Describe the morphology of the erythrocytes.
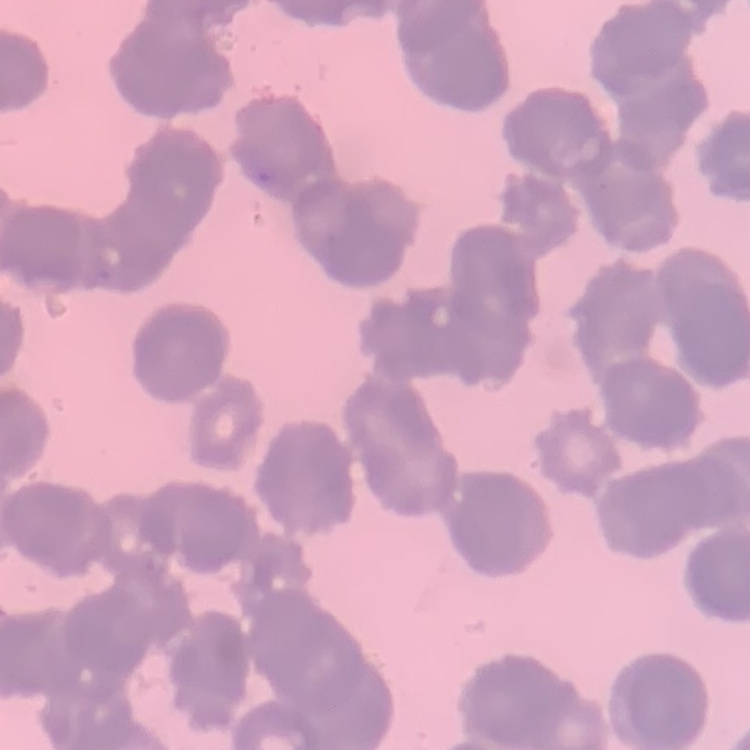
Rouleaux formation.

stain = Field's or Giemsa
preparation = thin blood smear
image type = one tile cut from a larger photomicrograph